Describe the morphology of the erythrocytes.
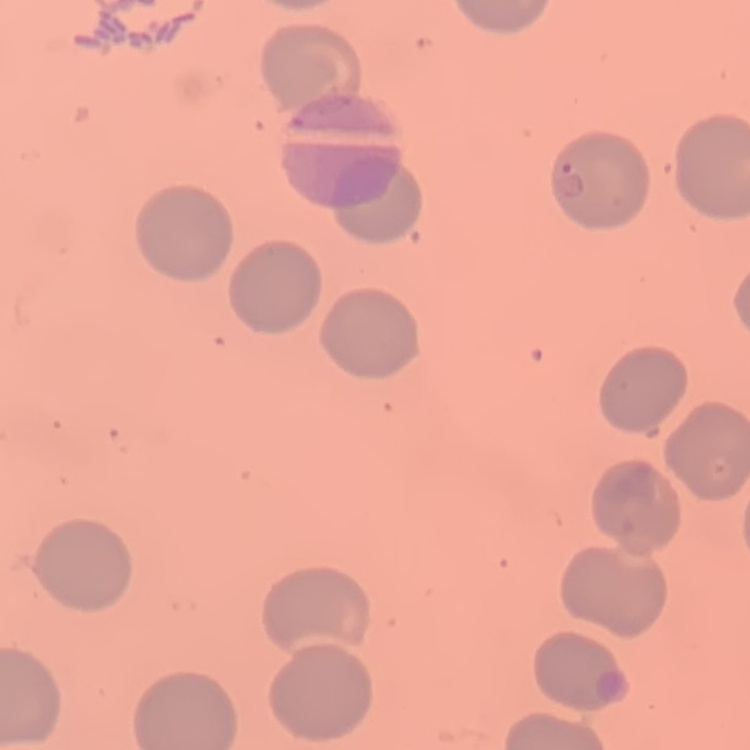

They show no rouleaux formation.

Stained with either Field's or Giemsa. Thin blood film. Square crop of a larger photomicrograph.